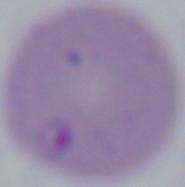

identification = Babesia
modality = photomicrograph
magnification = 1000x